Point out each leukocyte.
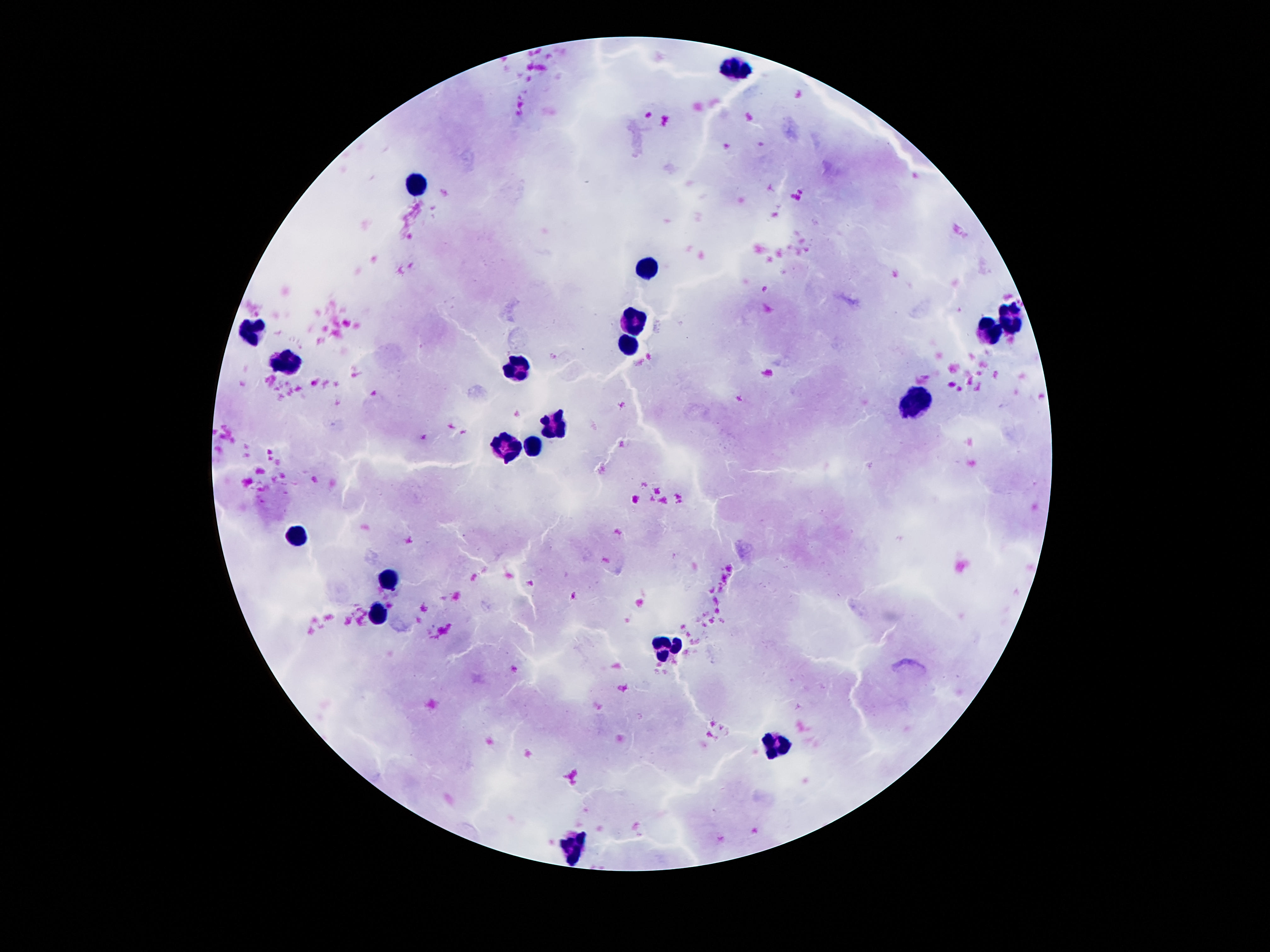

Approximate object centers, in pixels from the top-left corner.
Leukocytes: (x=737, y=66), (x=412, y=185), (x=643, y=267), (x=1010, y=318), (x=636, y=322), (x=249, y=332), (x=987, y=332), (x=628, y=343), (x=287, y=361), (x=521, y=366), (x=916, y=405), (x=552, y=422), (x=531, y=443), (x=506, y=445), (x=297, y=534), (x=389, y=580), (x=378, y=617), (x=661, y=649), (x=776, y=748), (x=574, y=846).

Patient malaria status: uninfected. Giemsa-stained preparation. 100x magnification. Thick peripheral-blood smear. One field from this slide. Photographed through the microscope eyepiece with a smartphone camera. Image is 1270×952 pixels.